Report the malaria status of this cell.
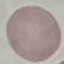
Uninfected.

Thin blood film. Photographed with a smartphone camera at the microscope eyepiece. Cell patch, automatically extracted from a larger field of view and resized to 64 × 64 pixels. Giemsa stain.